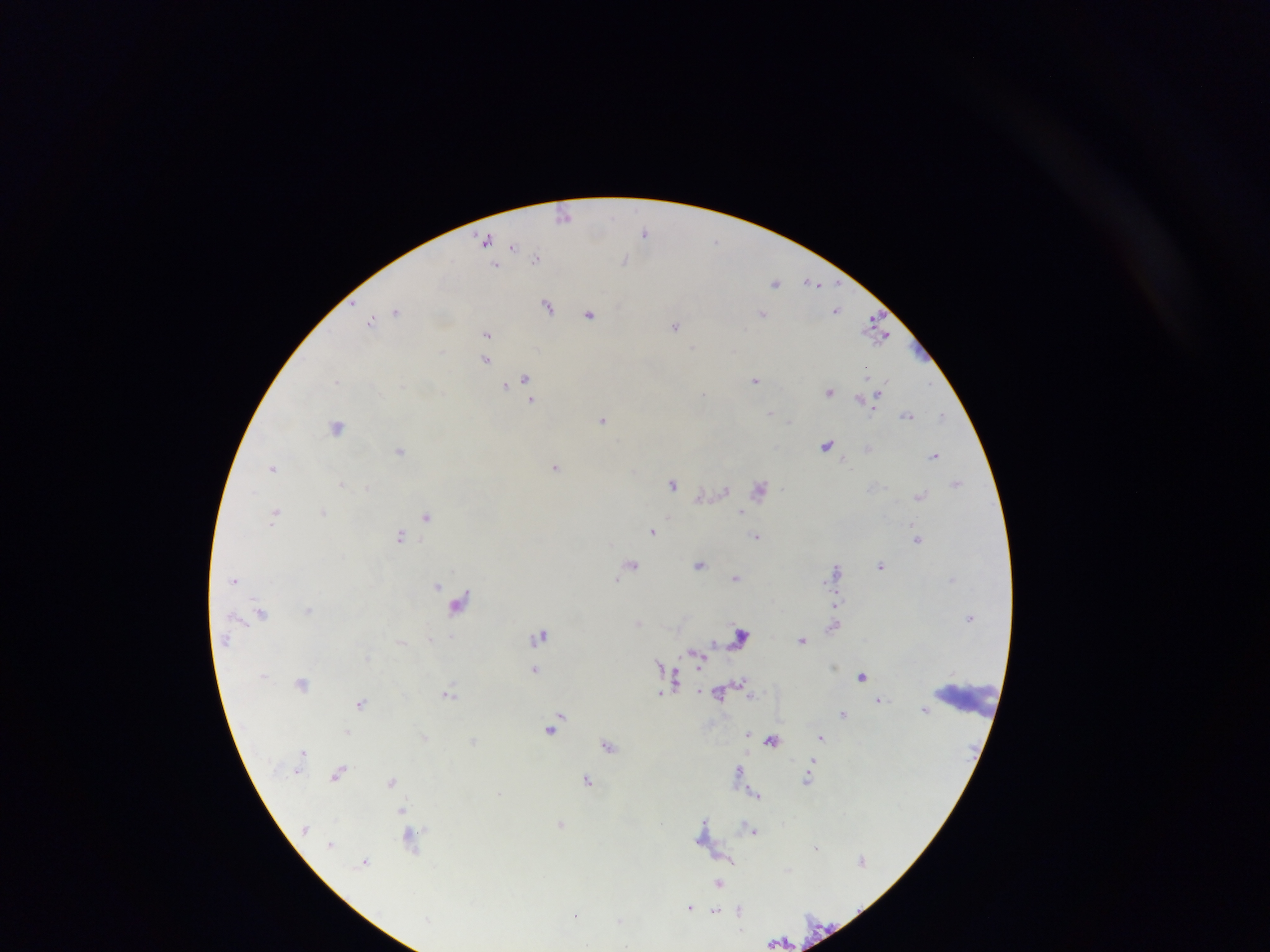
Approximate centers as [x, y] in pixels. Leukocyte locations: [967, 698]. Plasmodium parasite locations: [565, 214], [646, 233], [487, 240], [514, 246], [538, 258], [626, 260], [497, 266], [776, 282], [813, 283], [548, 304], [838, 309], [395, 311], [590, 312], [763, 315], [372, 321], [676, 326], [877, 326], [487, 334], [486, 360], [526, 377], [756, 380], [505, 385], [830, 390], [704, 392], [878, 395], [863, 399], [868, 399], [532, 401], [906, 415], [942, 415], [603, 419], [339, 425], [827, 444], [401, 449], [869, 449], [935, 455], [555, 466], [274, 467], [342, 483], [957, 483], [673, 484], [760, 488], [725, 490], [920, 495], [701, 496], [741, 511], [275, 512], [323, 512], [426, 516], [653, 530], [757, 535], [401, 536], [918, 538], [632, 564], [700, 564], [882, 566], [837, 571], [736, 577], [235, 581], [439, 584], [460, 602], [836, 605], [308, 609], [262, 613], [639, 622], [834, 625], [741, 633], [542, 634], [803, 639], [402, 640], [698, 656], [536, 669], [862, 675], [675, 677], [303, 682], [742, 682], [720, 691], [449, 692], [661, 693], [879, 700], [361, 702], [925, 709], [845, 713], [553, 726], [349, 731], [749, 733], [424, 736], [822, 737], [473, 741], [773, 741], [609, 744], [305, 750], [814, 760], [740, 770], [338, 773], [807, 779], [588, 780], [391, 781], [757, 793], [401, 810], [561, 822], [751, 831], [703, 832], [411, 837], [863, 860], [366, 861], [719, 882], [690, 908], [739, 910], [716, 911], [577, 915], [779, 940]. Sample from Ghana. Thick blood film. Photographed through a microscope with a mobile-phone camera. Image is 1270×952 pixels. One field of view.